Locate every blood parasite and identify its species.
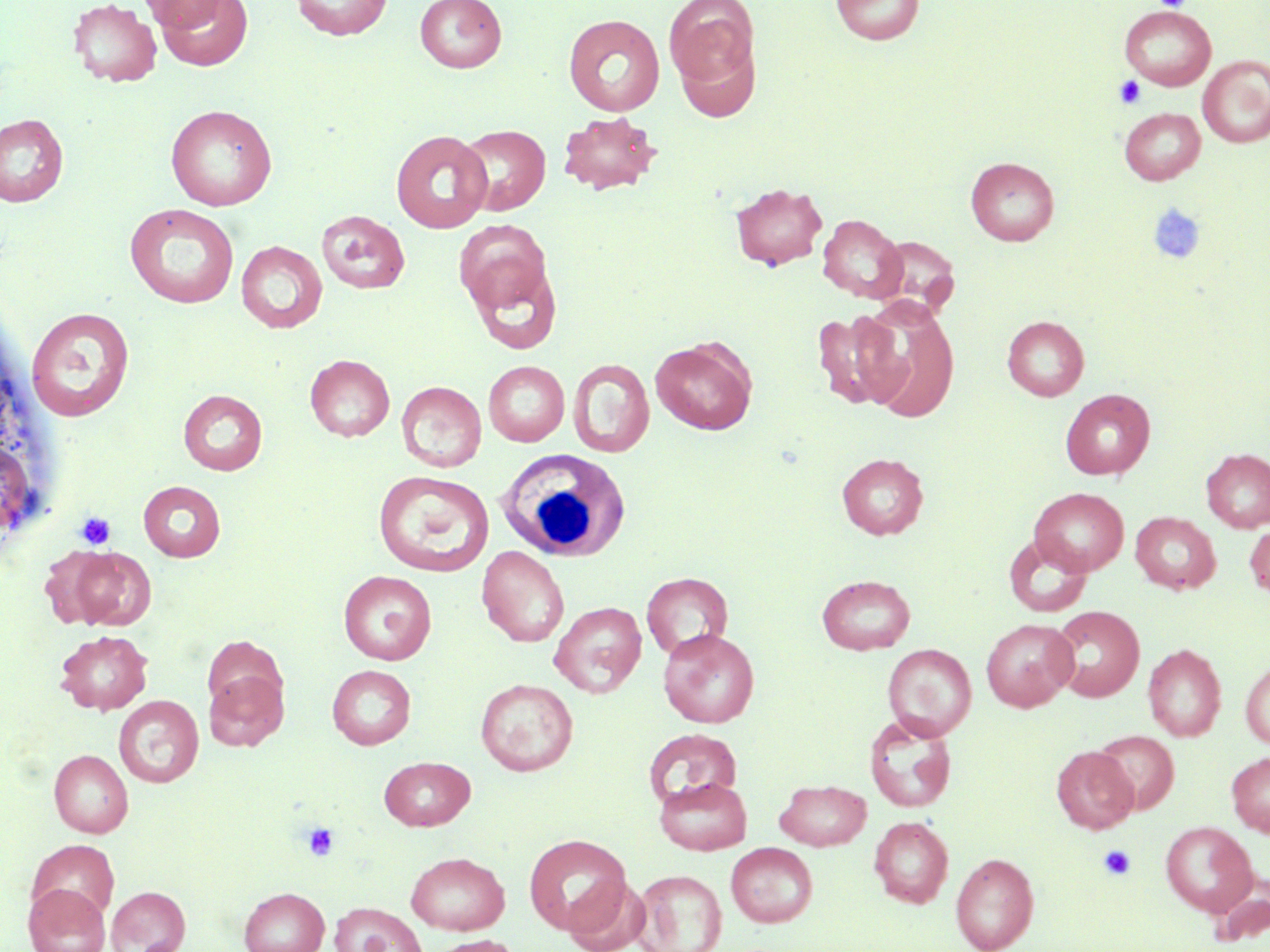

No blood parasites seen.

Summary:
  - Coordinate format: approximate bounding boxes as (x1,y1)-(x2,y2) corner pairs in pixels
  - Uninfected red blood cell locations: (67,0)-(162,88), (138,0)-(230,32), (154,0)-(253,71), (291,0)-(393,40), (415,0)-(507,72), (664,0)-(760,98), (830,1)-(924,45), (1120,6)-(1216,90), (563,14)-(666,116), (1198,55)-(1270,148), (165,105)-(277,211), (1119,107)-(1206,185), (557,111)-(662,196), (0,113)-(69,207), (457,124)-(551,216), (390,130)-(493,233), (965,157)-(1060,246), (730,182)-(828,271), (124,204)-(239,309), (316,210)-(409,294), (817,214)-(907,303), (453,218)-(554,317), (870,235)-(960,318), (236,240)-(328,333), (465,259)-(563,354), (857,299)-(960,423), (26,307)-(135,422), (813,308)-(906,411), (1002,315)-(1089,400), (650,337)-(757,434), (305,354)-(395,441), (568,358)-(654,458), (483,361)-(569,447), (396,381)-(487,473), (1060,388)-(1155,479), (179,389)-(268,475), (1201,448)-(1270,532), (837,452)-(929,540), (0,453)-(33,533), (374,470)-(494,576), (138,481)-(226,561), (1029,487)-(1129,576), (1131,512)-(1220,593), (1245,522)-(1270,599), (1004,534)-(1093,617), (477,545)-(569,647), (66,547)-(157,630), (338,570)-(437,665), (641,572)-(733,660), (816,574)-(916,654), (549,601)-(647,698), (1049,605)-(1144,702), (980,619)-(1078,711), (658,628)-(760,728), (54,629)-(153,715), (1143,643)-(1226,741), (883,644)-(977,741), (1240,658)-(1270,749), (326,664)-(416,749), (203,669)-(289,751), (475,678)-(578,776), (113,695)-(204,788), (864,713)-(957,813), (643,727)-(743,807), (1092,729)-(1180,814), (1051,746)-(1138,833), (49,749)-(133,837), (1227,751)-(1270,837), (379,756)-(475,831), (655,777)-(751,855), (775,779)-(871,850), (869,816)-(953,908), (1160,821)-(1257,917), (523,833)-(631,934), (26,839)-(120,922), (726,842)-(818,928), (405,852)-(510,935), (950,852)-(1038,952), (633,869)-(728,952), (1208,872)-(1269,946), (563,875)-(652,952), (23,883)-(111,952), (106,886)-(191,952), (239,887)-(330,952), (329,901)-(426,952), (427,935)-(523,952)
  - Platelet locations: (1154,0)-(1191,11), (1113,75)-(1146,108), (1147,204)-(1206,265), (75,512)-(116,550), (301,822)-(339,861), (1098,844)-(1137,882)
  - White blood cell locations: (493,448)-(634,568)
  - Slide-level diagnosis: no evidence of blood parasites
  - Modality: light microscopy
  - Image size: 1270×952 pixels
  - Preparation: thin blood smear
  - Magnification: 1000x
  - Stain: May-Grünwald-Giemsa
  - Field of view: single